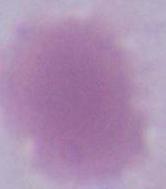

{
  "modality": "photomicrograph",
  "identification": "erythrocyte",
  "magnification": "1000x"
}